Give the position of every Plasmodium parasite visible.
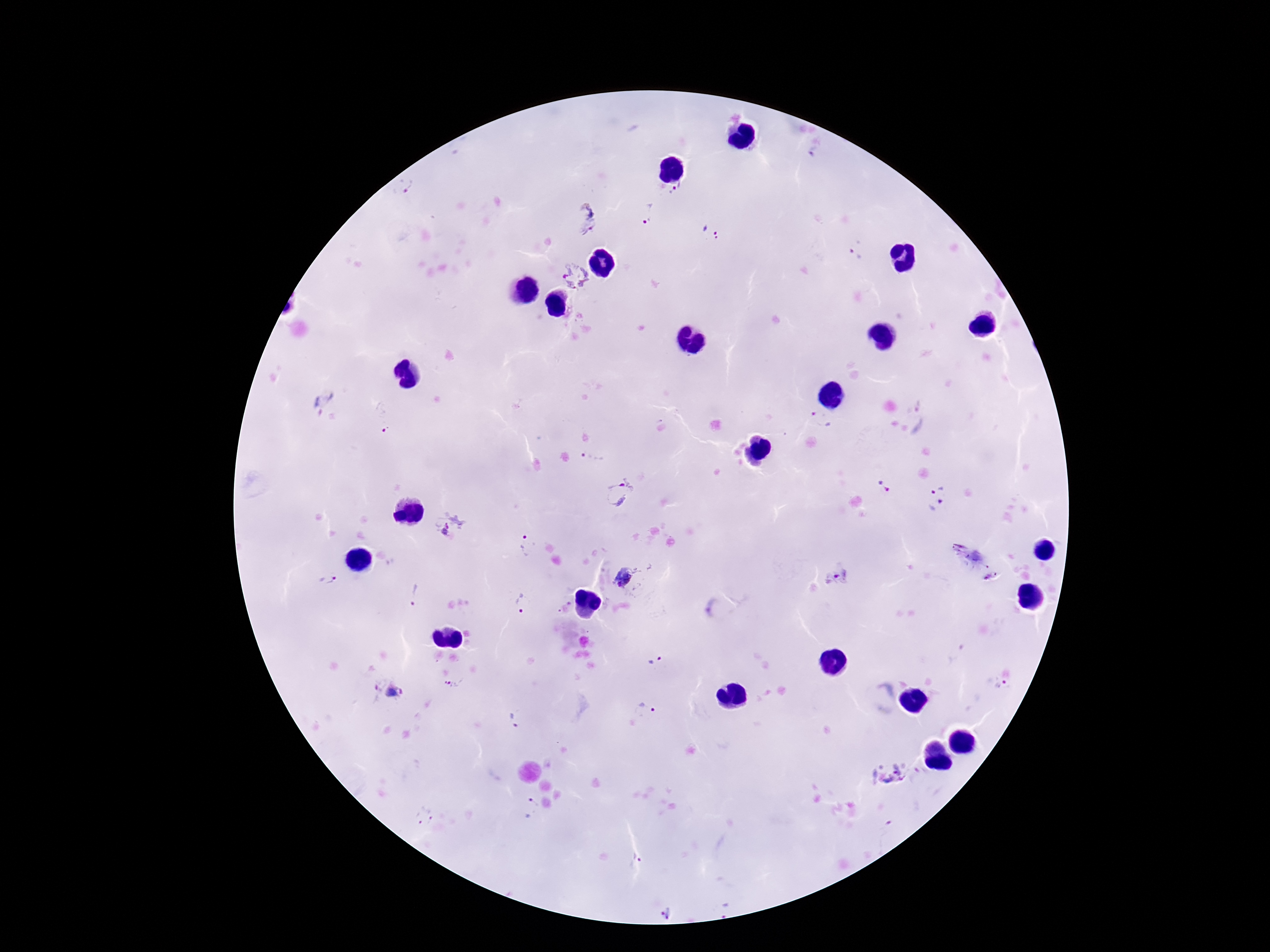

Approximate centers as [x, y] in pixels.
Plasmodium parasites: [676, 190], [406, 192], [649, 215], [586, 220], [711, 232], [855, 255], [574, 275], [321, 402], [381, 417], [821, 420], [593, 458], [885, 486], [937, 486], [618, 493], [939, 504], [449, 524], [525, 546], [627, 576], [838, 576], [330, 581], [415, 594], [523, 602], [656, 661], [454, 684], [1003, 688], [384, 694], [644, 709], [512, 719], [893, 774], [529, 807], [421, 816], [636, 860], [725, 910], [665, 913].

capture = smartphone camera through the microscope eyepiece
field of view = single
stain = Giemsa
preparation = thick blood smear
magnification = 100x
patient malaria status = positive
image size = 1270×952 pixels